Give the position of every leukocyte visible.
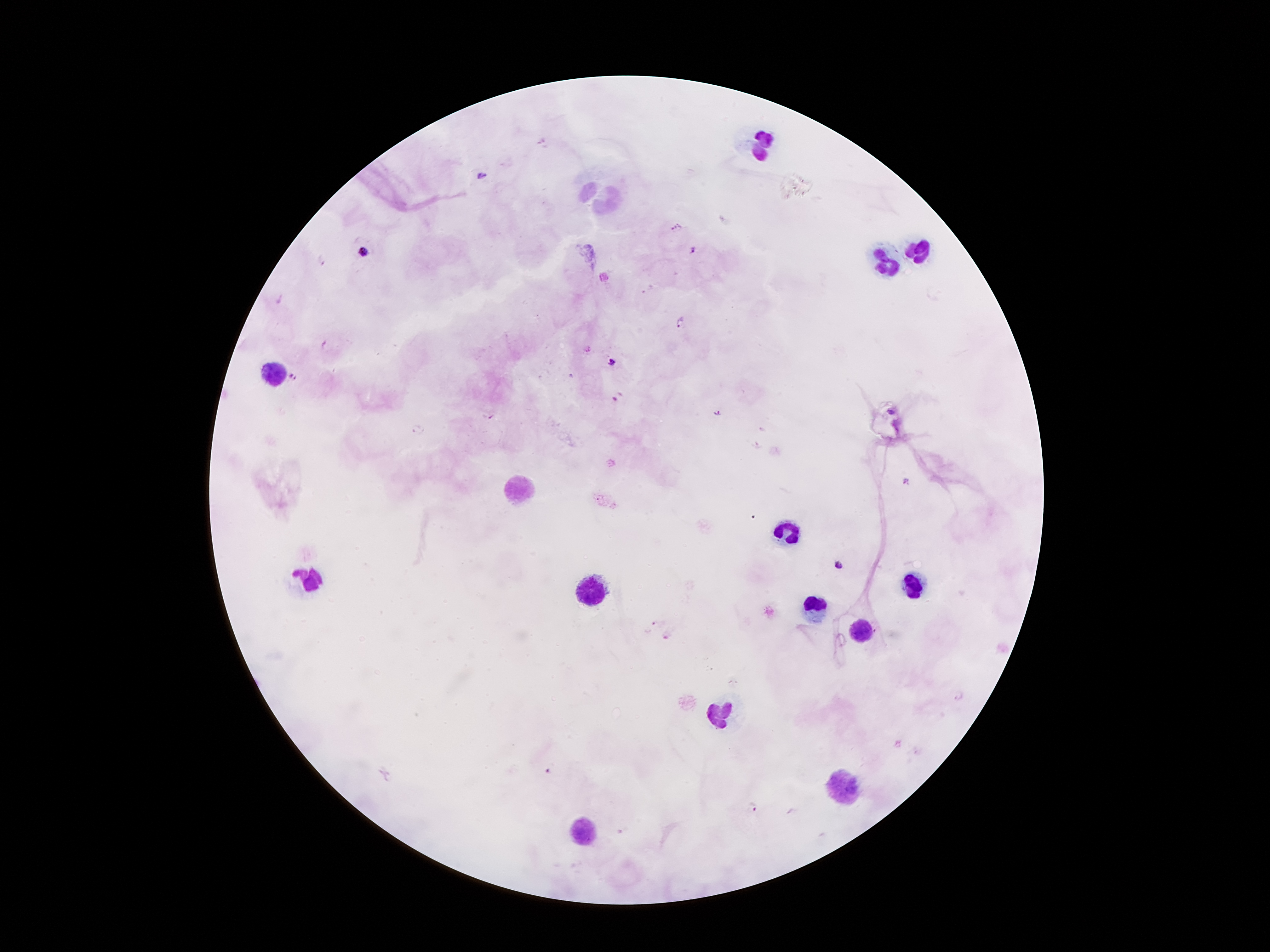
Approximate centers as [x, y] in pixels.
Leukocytes: [764, 144], [919, 249], [889, 263], [277, 372], [519, 488], [789, 532], [305, 578], [911, 582], [591, 591], [813, 607], [860, 631], [719, 715], [841, 784], [581, 829].

Summary:
  - Malaria parasite locations: [482, 174], [676, 228], [364, 249], [693, 251], [322, 261], [679, 321], [324, 343], [611, 361], [293, 377], [615, 399], [891, 412], [718, 413], [492, 417], [416, 429], [905, 480], [837, 564], [656, 623], [666, 635], [958, 694], [550, 770], [755, 806]
  - Capture: smartphone camera through the microscope eyepiece
  - Preparation: thick blood film
  - Patient malaria status: infected with Plasmodium falciparum
  - Stain: Giemsa
  - Field of view: one from this slide
  - Magnification: 100x
  - Image size: 1270×952 pixels